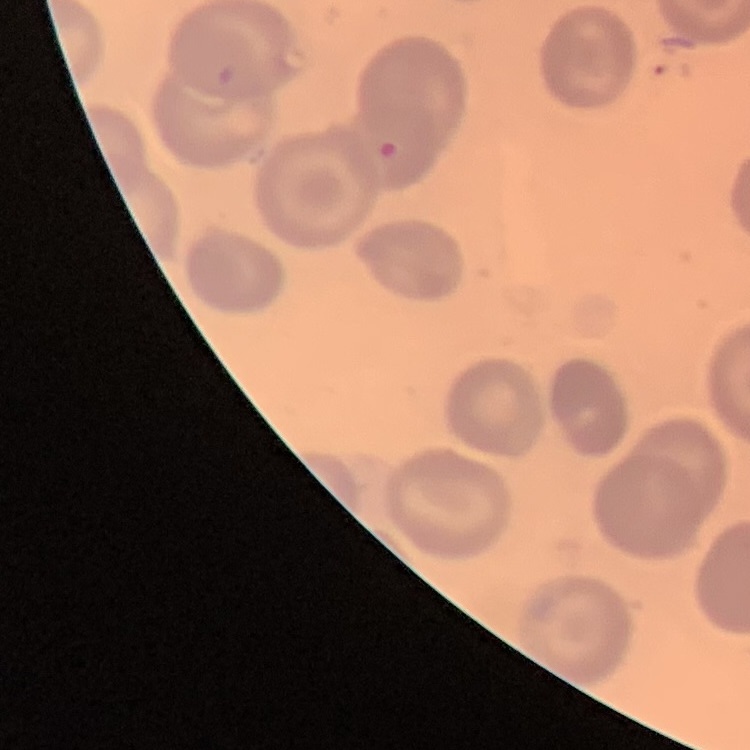 The red blood cells show no rouleaux formation. Stained with either Field's or Giemsa. Thin blood smear. Square crop of a larger photomicrograph.